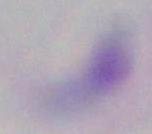

Captured at 1000x magnification. Micrograph. Toxoplasma gondii is shown.